Locate every Plasmodium parasite.
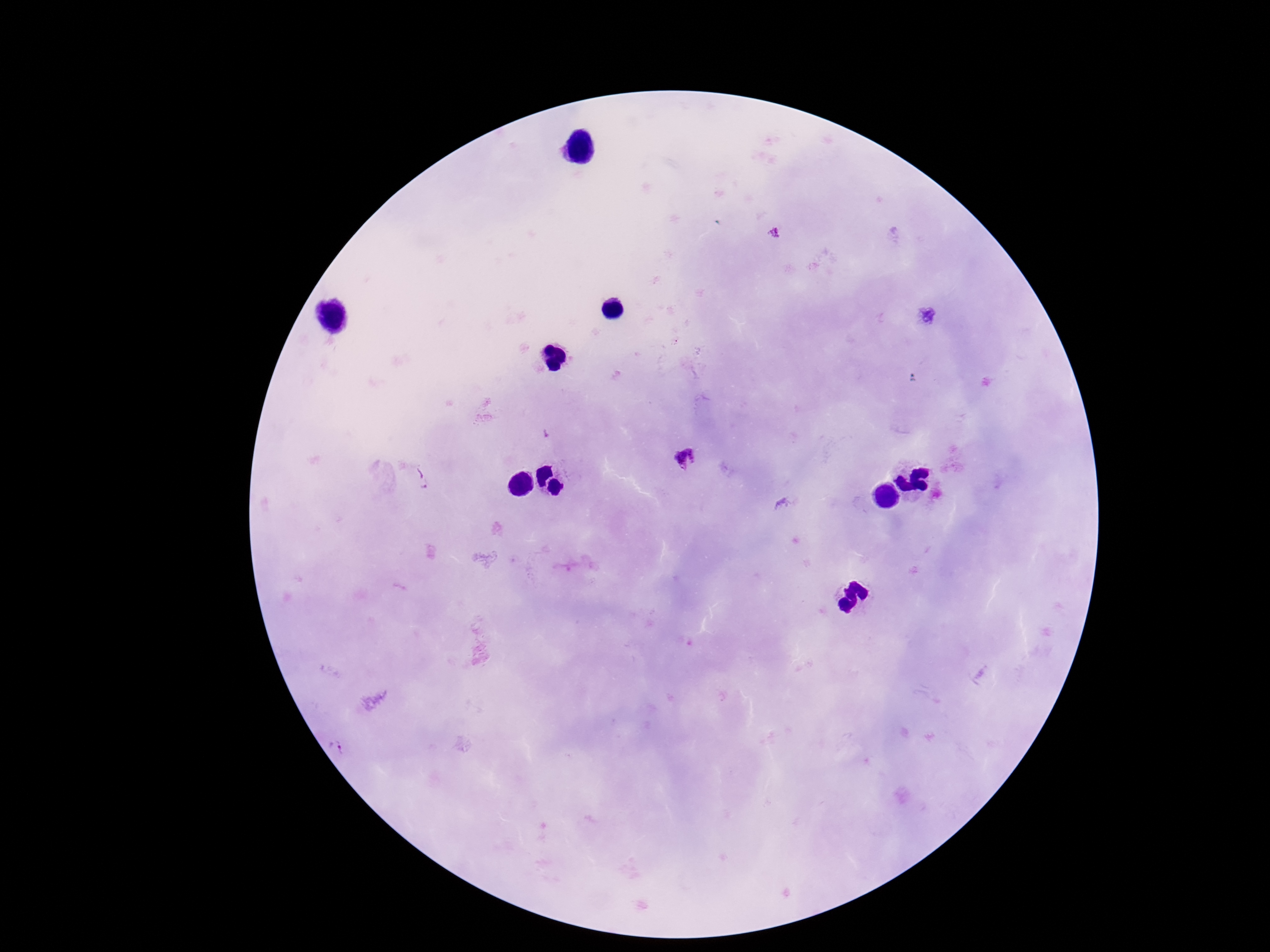

Approximate centers as (x, y) in pixels.
Plasmodium parasites: (775, 230), (547, 434), (686, 459), (421, 478), (340, 742).

Summary:
  - Stain: Giemsa
  - Image size: 1270×952 pixels
  - Capture: smartphone camera through the microscope eyepiece
  - Preparation: thick blood smear
  - Magnification: 100x
  - Patient malaria status: positive
  - Field of view: single